Identify the preparation type.
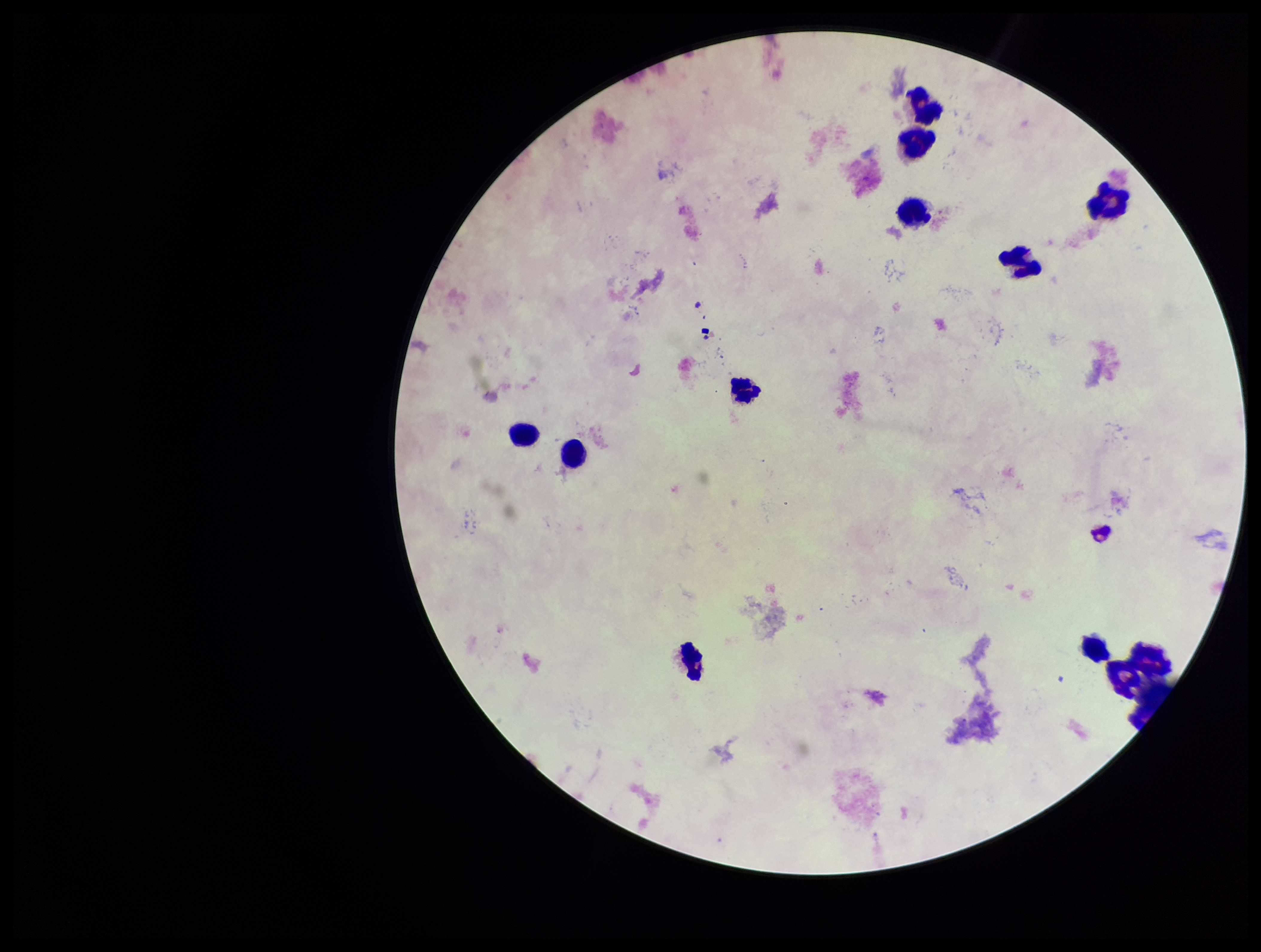

Thick.

Summary:
  - Plasmodium parasites: none detected
  - Stain: Giemsa
  - Leukocyte count: 10
  - Image size: 1261×952 pixels
  - Species reported for this patient: Plasmodium falciparum
  - Parasite count: 0
  - Capture: smartphone photograph through the microscope eyepiece
  - Field of view: one from this slide
  - Patient malaria status: infected